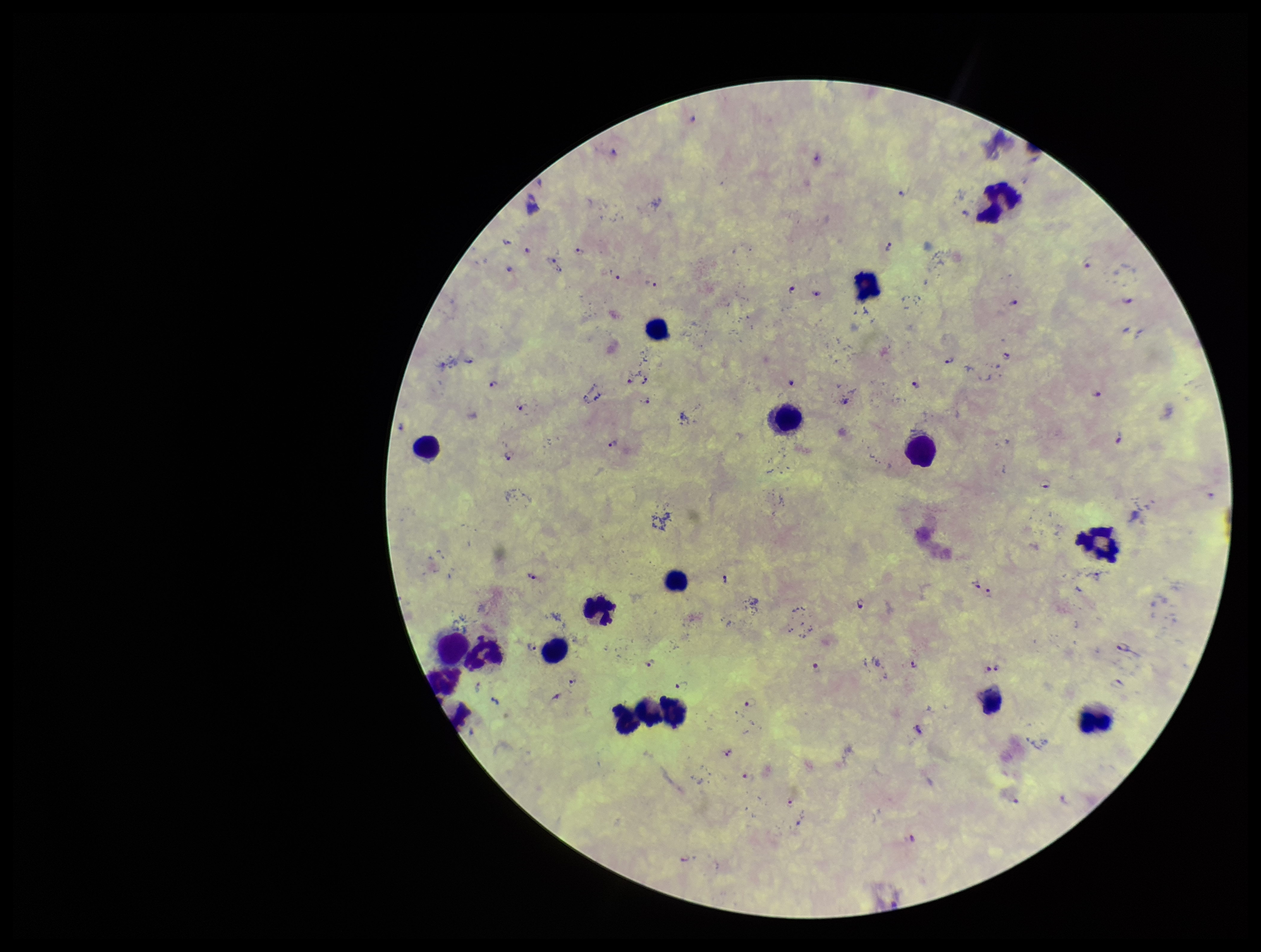
Summary:
  - Species reported for this patient: Plasmodium falciparum
  - Patient malaria status: infected
  - Capture: smartphone photograph through the microscope eyepiece
  - Parasite count: 65
  - Preparation: thick smear
  - Image size: 1261×952 pixels
  - Leukocyte count: 18
  - Plasmodium parasites: detected
  - Stain: Giemsa
  - Field of view: one from this slide